Name the cell type shown.
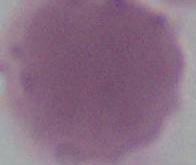
An erythrocyte.

Summary:
  - Magnification: 1000x
  - Modality: photomicrograph